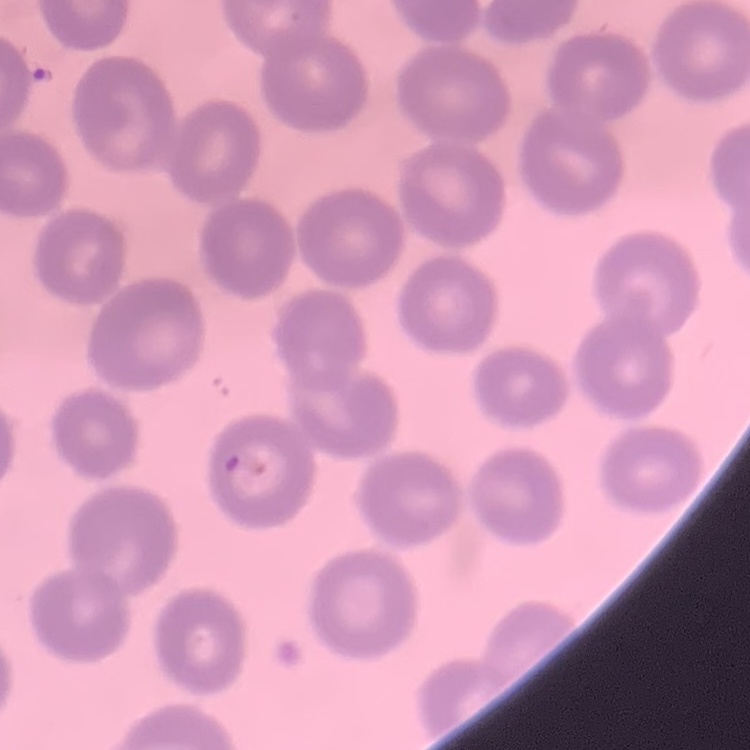 The red blood cells exhibit no rouleaux formation. One tile cut from a larger photomicrograph. Thin peripheral smear. Field's or Giemsa stain.